Point out each Plasmodium parasite.
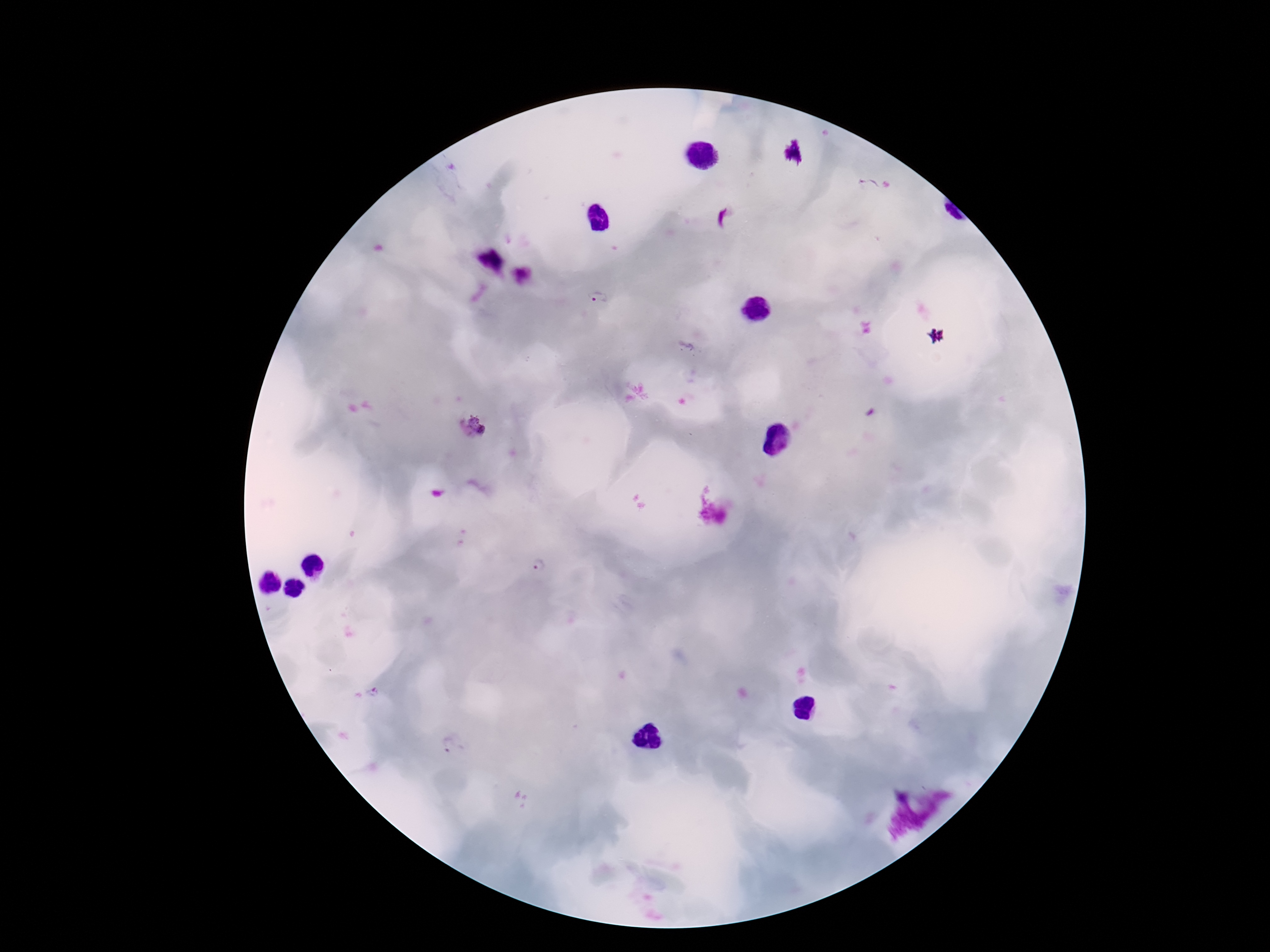

Approximate centers as [x, y] in pixels.
Plasmodium parasites: [868, 185], [599, 298], [472, 429], [537, 561], [455, 746].

Summary:
  - Magnification: 100x
  - Capture: smartphone camera through the microscope eyepiece
  - Preparation: thick blood smear
  - Image size: 1270×952 pixels
  - Field of view: single
  - Stain: Giemsa
  - Patient malaria status: positive